State the blood parasite species.
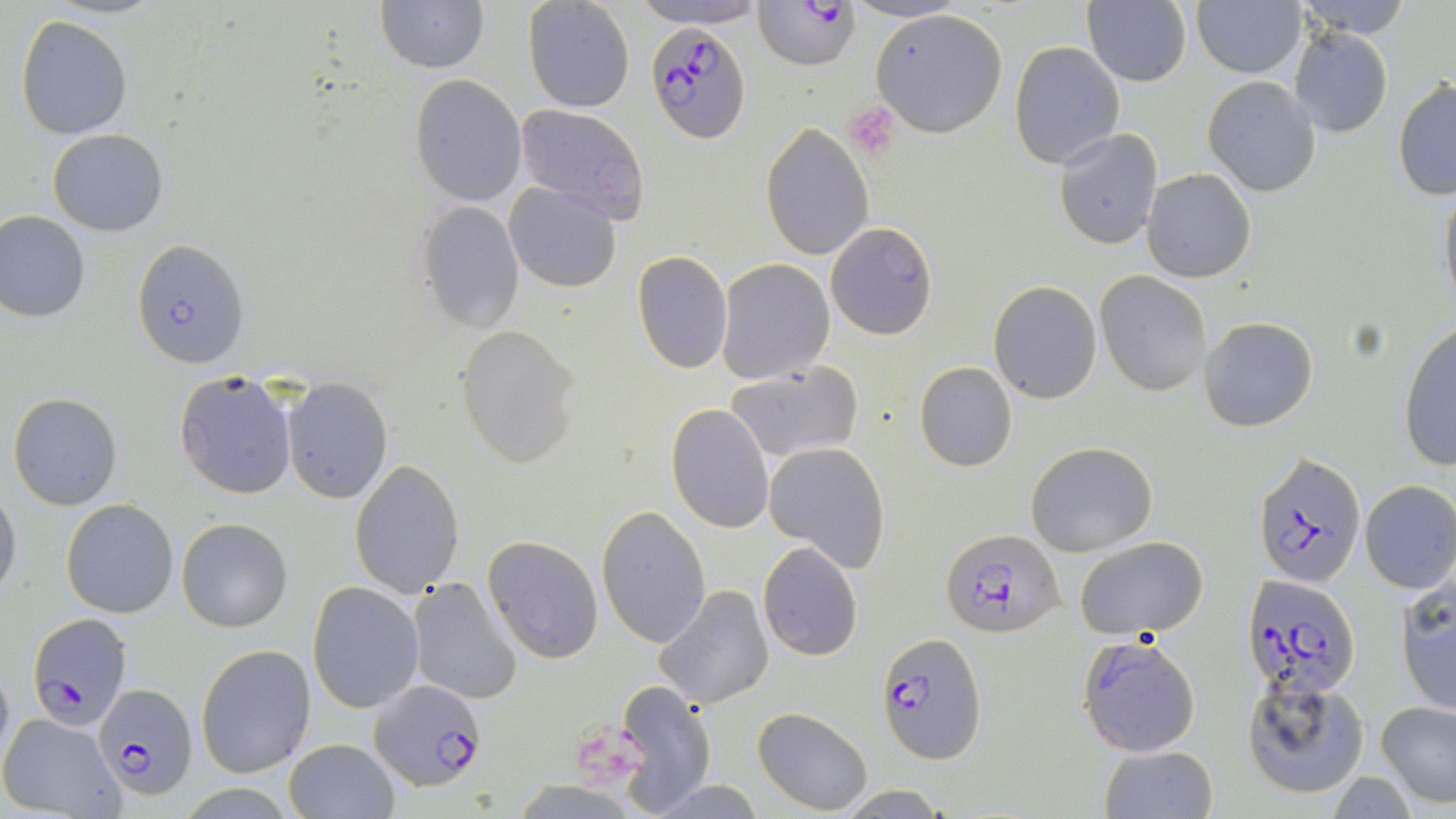

Plasmodium falciparum.

Approximate bounding boxes as (x1, y1, x2, y2) in pixels. Platelet locations: (844, 101, 902, 157). Plasmodium falciparum-infected red blood cell locations: (756, 1, 861, 70), (648, 21, 752, 143), (133, 239, 249, 367), (1253, 452, 1368, 591), (940, 528, 1064, 638), (1244, 575, 1361, 701), (28, 612, 131, 728), (877, 634, 987, 762), (1077, 634, 1202, 757), (371, 679, 486, 791), (96, 683, 198, 801). Uninfected red blood cell locations: (45, 0, 162, 20), (375, 0, 489, 73), (1084, 0, 1193, 88), (1293, 0, 1413, 41), (522, 1, 634, 114), (630, 1, 769, 28), (1192, 1, 1306, 78), (869, 8, 1009, 138), (14, 14, 134, 141), (1288, 27, 1393, 139), (1008, 42, 1125, 168), (408, 75, 527, 206), (1203, 77, 1322, 196), (1392, 79, 1456, 200), (513, 105, 651, 226), (761, 123, 875, 260), (47, 129, 167, 236), (1053, 131, 1162, 249), (1140, 168, 1256, 284), (503, 180, 623, 293), (1438, 186, 1456, 307), (417, 198, 525, 332), (0, 211, 90, 324), (825, 222, 938, 341), (632, 251, 733, 374), (716, 259, 834, 385), (1097, 272, 1212, 395), (989, 281, 1101, 404), (1198, 316, 1318, 431), (1398, 320, 1456, 470), (453, 325, 579, 466), (913, 361, 1019, 472), (726, 363, 865, 462), (174, 371, 297, 500), (282, 380, 392, 502), (8, 393, 121, 510), (664, 404, 775, 534), (1025, 441, 1157, 555), (764, 443, 892, 572), (350, 460, 464, 597), (1360, 480, 1456, 595), (0, 485, 21, 598), (60, 499, 178, 618), (596, 505, 712, 648), (177, 518, 293, 632), (481, 535, 603, 664), (1073, 536, 1208, 640), (757, 543, 862, 661), (407, 576, 522, 705), (1394, 577, 1455, 717), (307, 582, 423, 714), (655, 585, 776, 708), (196, 644, 317, 778), (1241, 677, 1370, 800), (615, 680, 717, 809), (1376, 700, 1456, 808), (752, 707, 872, 813), (0, 710, 126, 818), (285, 737, 399, 818), (1098, 745, 1218, 819). Image is 1456×819 pixels. Optical microscopy. Thin blood smear. 1000x magnification. May-Grünwald-Giemsa stain. Single field of view.